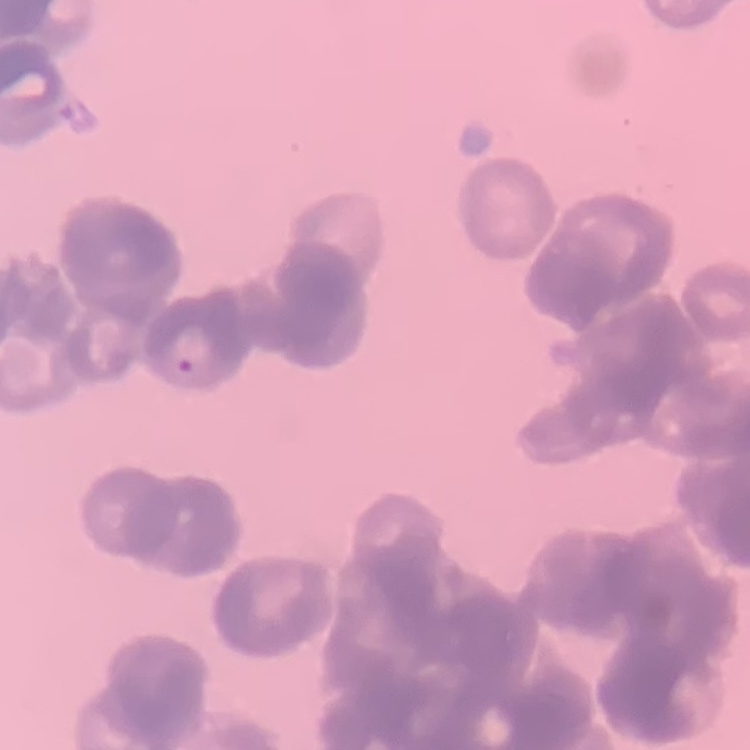

The erythrocytes exhibit rouleaux formation. Field's or Giemsa stain. Square crop of a larger photomicrograph. Thin peripheral smear.